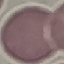

Summary:
  - Result: no malaria parasites detected
  - Preparation: thin blood film
  - Image type: automatically extracted cell patch, resized to 64 × 64 pixels
  - Capture: smartphone camera at the microscope eyepiece
  - Stain: Giemsa